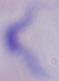

identification = trypanosome
modality = micrograph
magnification = 1000x